Describe the morphology of the red blood cells.
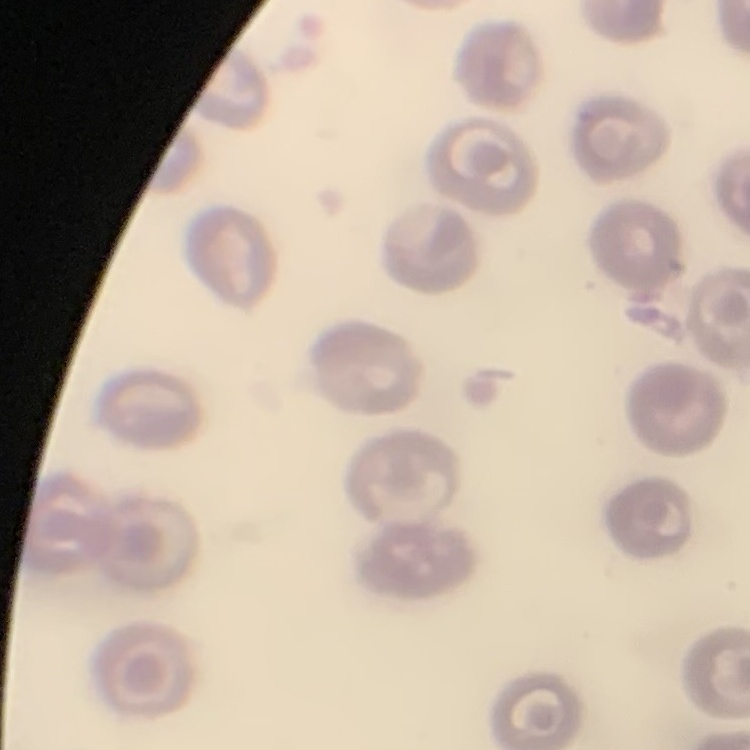
They show no rouleaux formation.

image type = square crop of a larger photomicrograph
stain = Field's or Giemsa
preparation = thin blood film